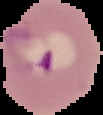
preparation: thin blood film
image_size: 103×115 pixels
malaria_status: parasitized
image_type: cell region segmented out of the field of view; surrounding area masked to black